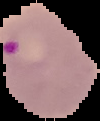

From a thin blood film. Image is 100×121 pixels. Result: Plasmodium parasites identified. The area outside the segmented cell region is set to black.